Assess this cell for malaria.
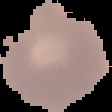

It is uninfected.

preparation = thin blood film
image type = segmented cell region with the area outside set to black
image size = 112×112 pixels